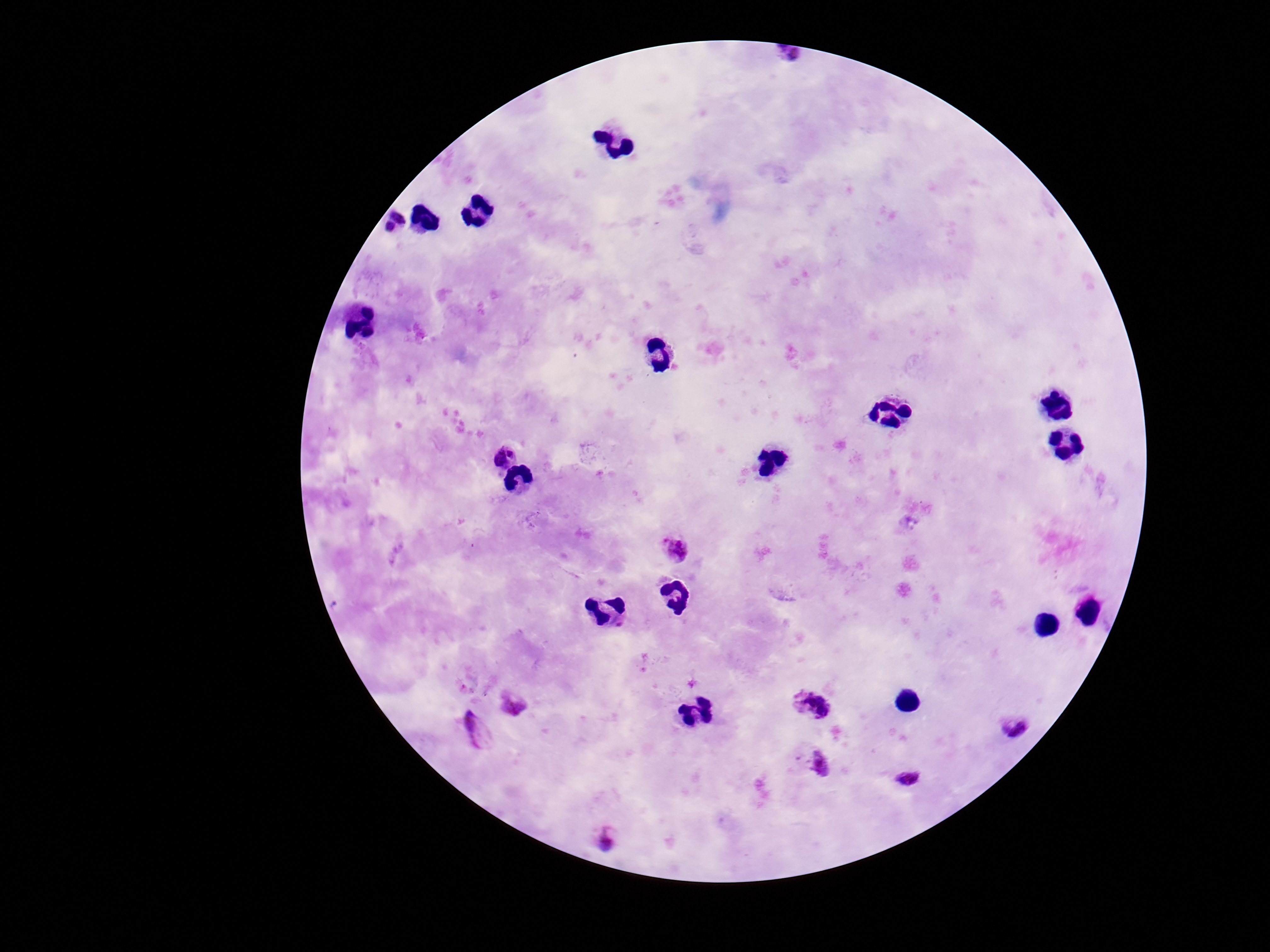

Approximate centers as [x, y] in pixels. Plasmodium parasite locations: [394, 222], [502, 452], [678, 549], [514, 703], [813, 705], [1013, 726], [472, 731], [820, 762], [908, 778], [604, 839]. Single field of view. Smartphone photograph taken through the microscope eyepiece. Patient malaria status: infected. Giemsa-stained preparation. Thick blood film. Image is 1270×952 pixels. 100x magnification.